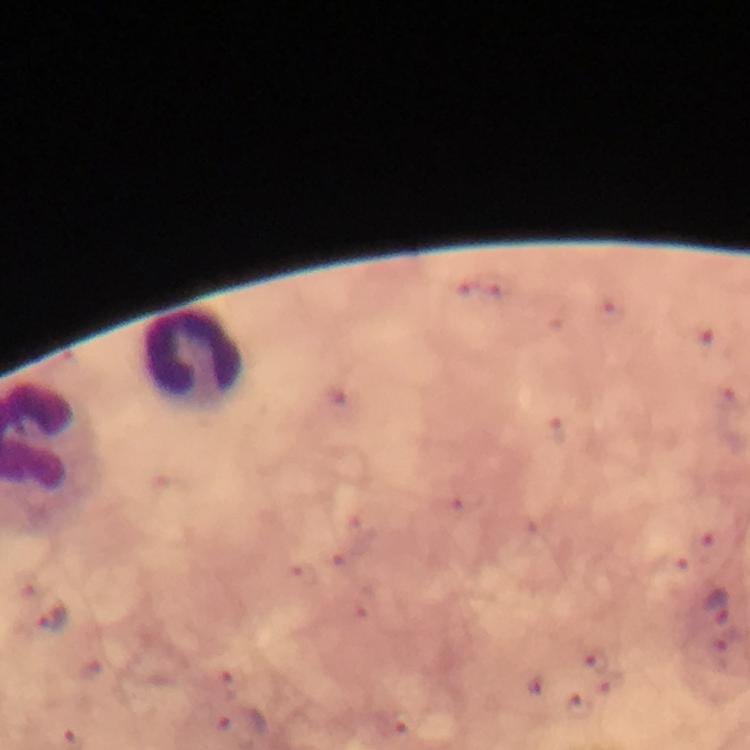
leukocyte locations = approximate object centers, in pixels from the top-left corner: (x=193, y=357)
capture = smartphone camera through the microscope
image size = 750×750 pixels
stain = Giemsa
immersion oil = applied
context = from a diagnostic examination for malaria
Plasmodium parasite locations = approximate object centers, in pixels from the top-left corner: (x=718, y=608), (x=49, y=619)
magnification = 100x
cropped from = a single field of view
preparation = thick blood smear